Point out each Plasmodium parasite.
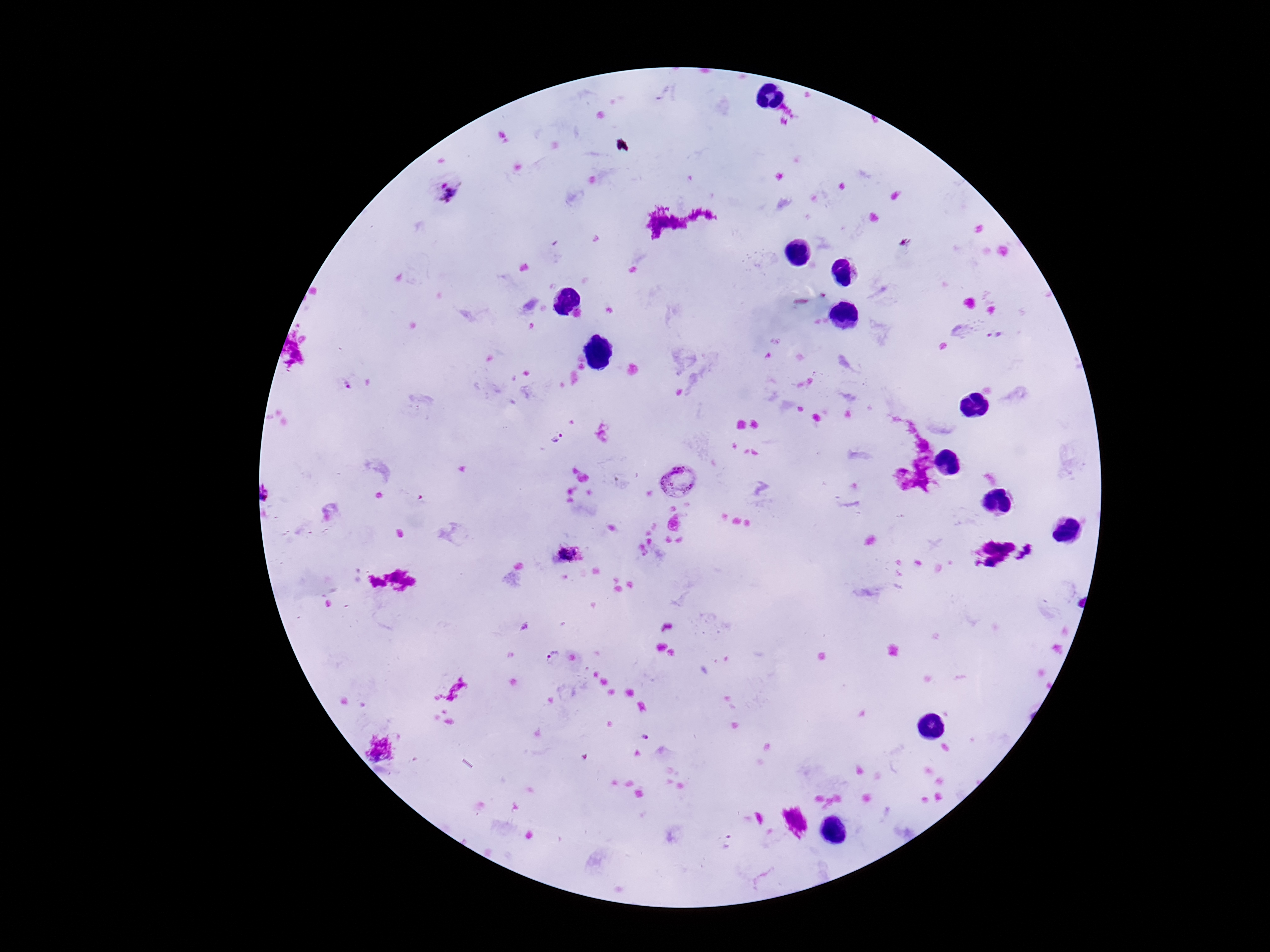
Approximate centers as {x, y} in pixels.
Plasmodium parasites: {444, 188}, {996, 335}, {345, 384}, {557, 437}, {679, 479}, {568, 553}, {552, 657}, {645, 738}, {727, 841}.

Summary:
  - Image size: 1270×952 pixels
  - Field of view: one from this slide
  - Preparation: thick peripheral-blood smear
  - Capture: smartphone camera through the microscope eyepiece
  - Magnification: 100x
  - Patient malaria status: positive
  - Stain: Giemsa